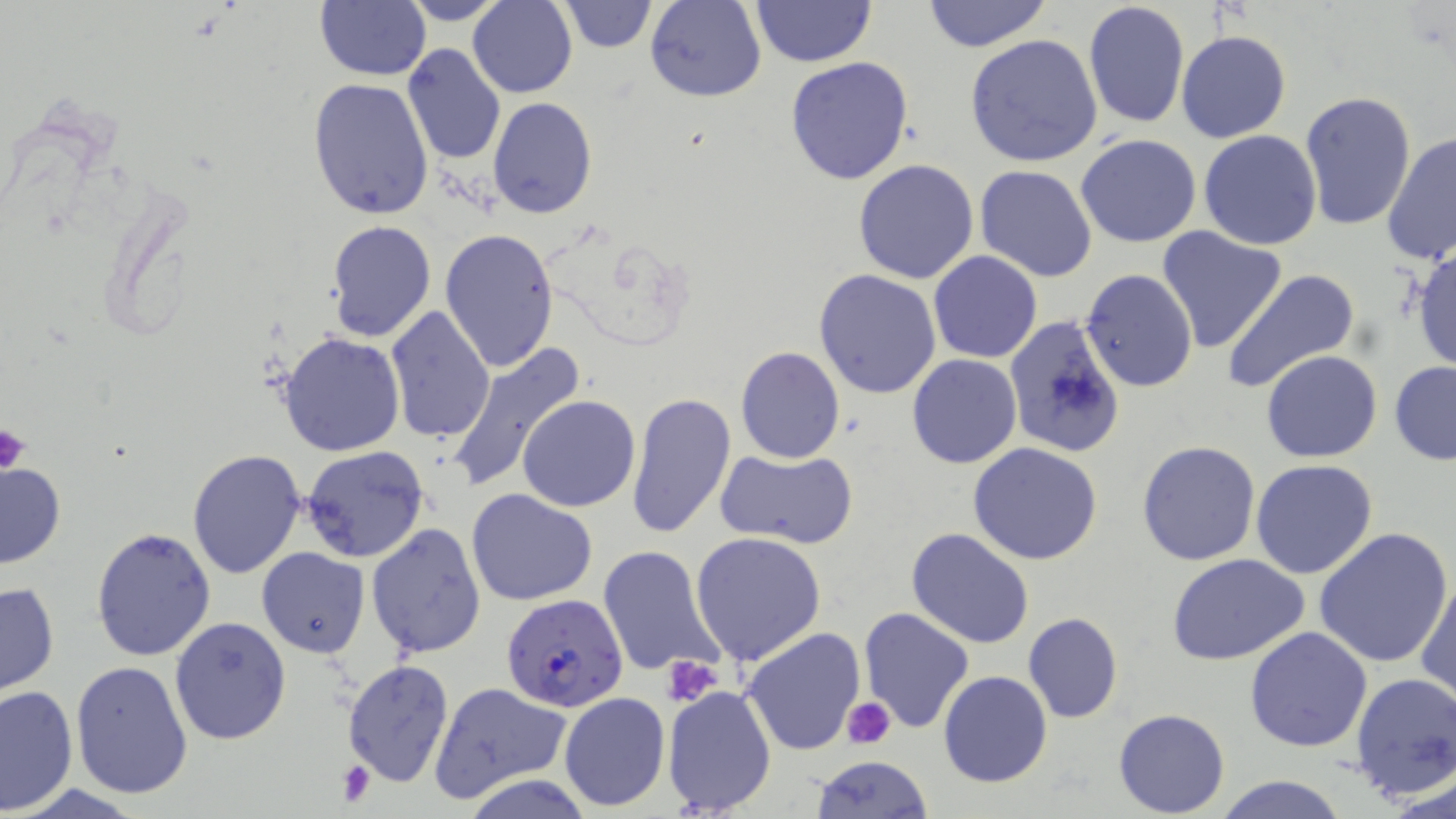
Approximate bounding boxes as (x1, y1, x2, y2) in pixels. Platelet locations: (1, 424, 31, 475), (662, 658, 725, 706), (842, 697, 896, 750), (336, 760, 379, 806). Plasmodium falciparum-infected red blood cell locations: (502, 596, 630, 711). Uninfected red blood cell locations: (315, 0, 431, 81), (396, 0, 508, 25), (467, 0, 578, 98), (645, 0, 765, 102), (922, 0, 1052, 52), (558, 1, 658, 53), (749, 1, 876, 67), (1082, 2, 1190, 131), (1176, 29, 1292, 144), (965, 34, 1103, 167), (400, 42, 506, 166), (785, 57, 914, 186), (308, 76, 434, 219), (1300, 90, 1417, 231), (487, 97, 598, 219), (1198, 129, 1323, 250), (1383, 130, 1455, 267), (1075, 133, 1202, 248), (852, 158, 980, 283), (974, 164, 1100, 282), (326, 220, 437, 343), (1157, 226, 1289, 354), (440, 227, 560, 371), (1409, 244, 1456, 373), (930, 251, 1042, 363), (1080, 268, 1199, 393), (1222, 268, 1361, 393), (814, 269, 942, 398), (385, 305, 496, 444), (1001, 315, 1126, 458), (278, 332, 406, 457), (444, 340, 587, 494), (735, 346, 844, 464), (1261, 349, 1383, 462), (907, 354, 1022, 468), (1388, 360, 1456, 466), (625, 393, 736, 539), (517, 394, 641, 512), (500, 408, 626, 597), (1136, 439, 1262, 567), (968, 443, 1102, 566), (301, 446, 431, 564), (187, 447, 307, 579), (716, 447, 859, 550), (1250, 459, 1378, 580), (0, 463, 64, 568), (468, 487, 598, 605), (366, 522, 487, 659), (906, 527, 1034, 649), (1313, 527, 1456, 669), (91, 528, 217, 662), (690, 531, 827, 666), (599, 544, 728, 680), (256, 547, 370, 658), (1165, 552, 1310, 666), (1415, 573, 1456, 703), (0, 579, 59, 698), (858, 606, 974, 734), (1022, 612, 1124, 724), (169, 616, 291, 743), (742, 626, 866, 755), (1244, 626, 1374, 752), (342, 658, 455, 789), (71, 661, 194, 800), (938, 670, 1053, 787), (1349, 672, 1456, 802), (429, 681, 570, 802), (0, 685, 78, 815), (662, 685, 777, 814), (558, 692, 670, 812), (1113, 708, 1230, 817), (809, 755, 933, 817), (461, 774, 596, 818), (1215, 774, 1349, 819). Slide-level diagnosis: Plasmodium falciparum. Optical microscopy. Thin blood smear. Image is 1456×819 pixels. May-Grünwald-Giemsa stain. 1000x magnification. Single field of view.